Give the position of every malaria parasite.
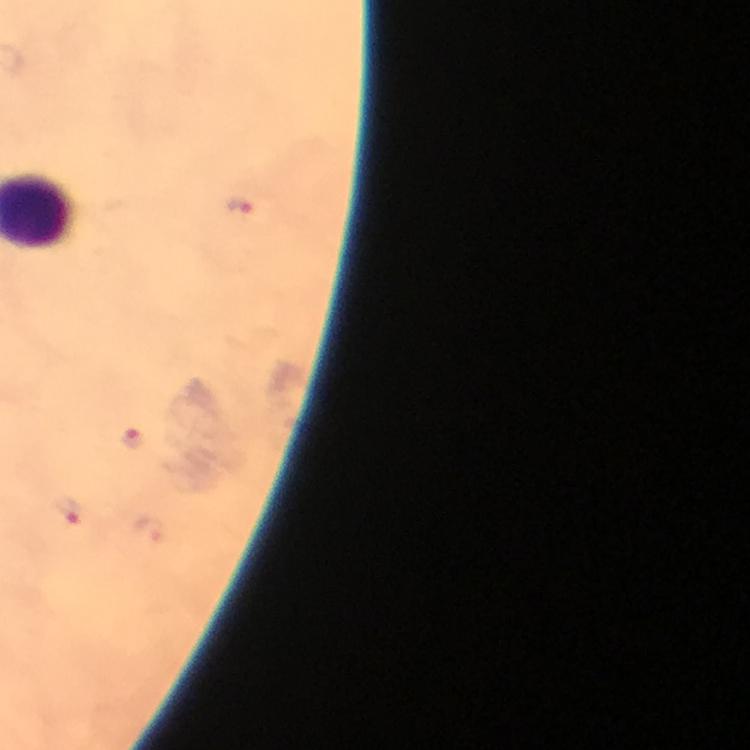
Approximate centers as [x, y] in pixels.
Malaria parasites: [240, 207], [134, 439], [69, 512].

context = from a malaria diagnostic workup
stain = Giemsa
preparation = thick blood film
capture = smartphone mounted on the microscope
image size = 750×750 pixels
immersion oil = applied
magnification = 100x
cropped from = a single field of view